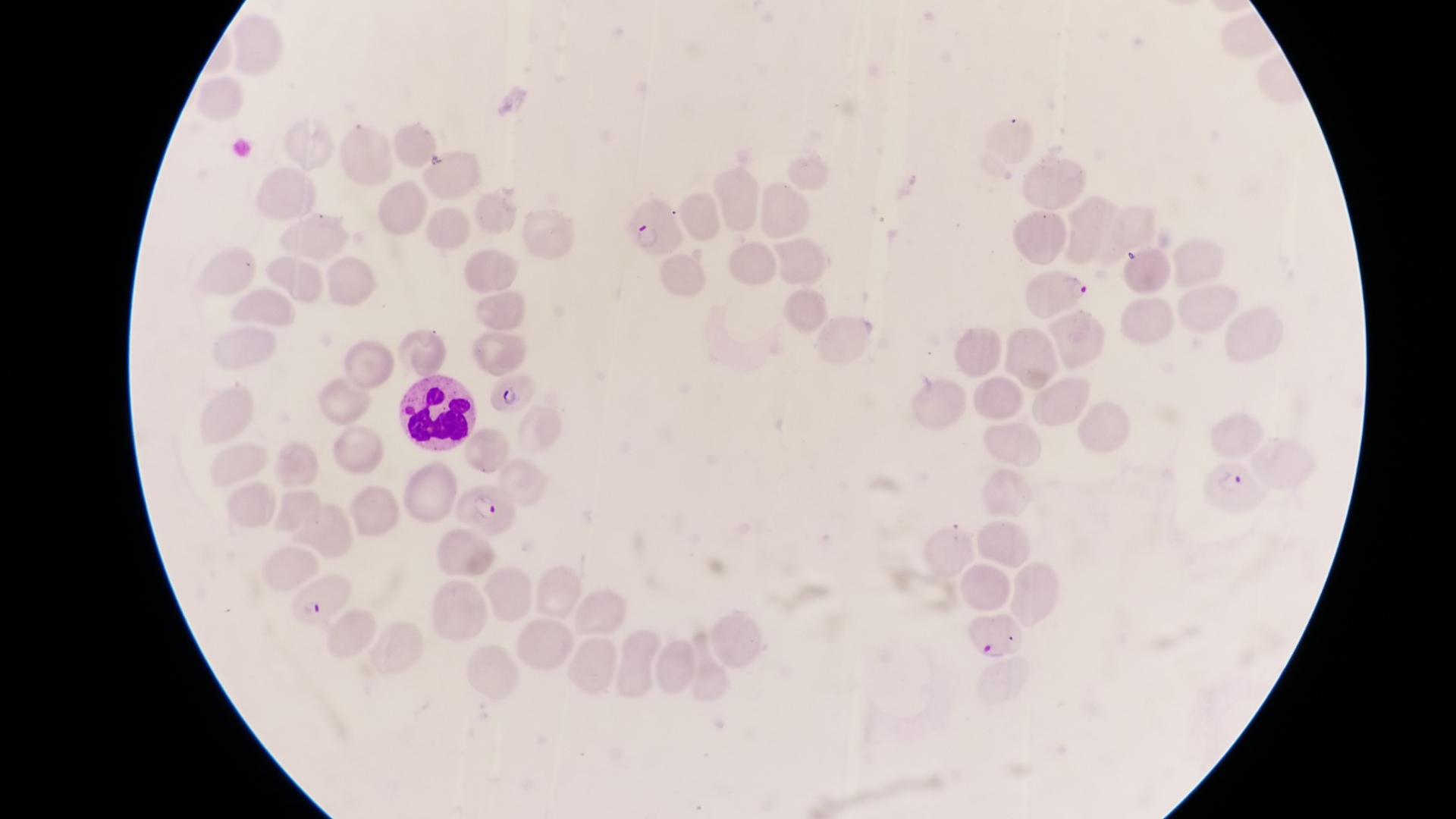

Approximate bounding boxes as (left, top, right, bottom) in pixels. Leukocyte locations: (397, 370, 480, 447). Parasitised red blood cell locations: (626, 201, 685, 256), (1026, 270, 1092, 320), (488, 373, 541, 413), (1203, 459, 1266, 522), (457, 486, 518, 541), (290, 565, 351, 621), (957, 608, 1023, 667). Image is 1456×819 pixels. Thin blood smear. Collected in Uganda. Captured by a smartphone held over the eyepiece of an Olympus CX-23 microscope. One field of view. Magnification of 1000x.